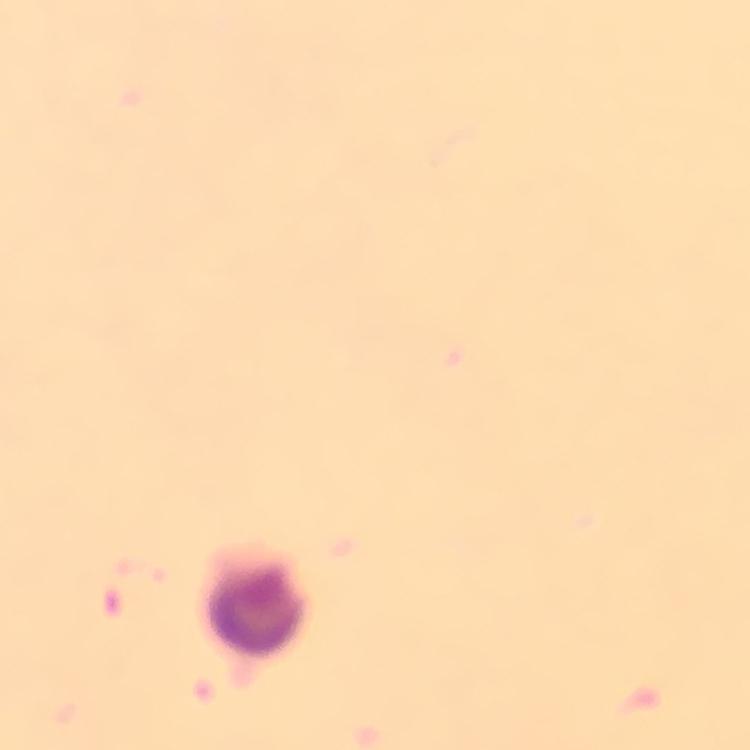

capture = smartphone mounted on the microscope
stain = Giemsa
preparation = thick blood smear
context = from a malaria diagnostic workup
immersion oil = applied
leukocyte locations = approximate centers as [x, y] in pixels: [255, 605]
cropped from = a single field of view
image size = 750×750 pixels
magnification = 100x
malaria parasites = none seen